Assess the morphology of the erythrocytes.
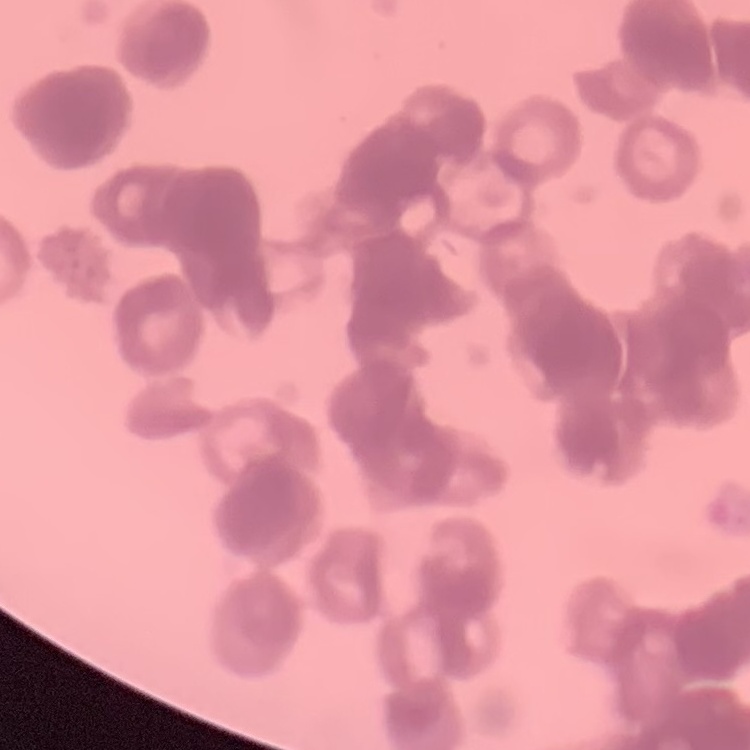
Rouleaux formation.

{
  "stain": "Field's or Giemsa",
  "image_type": "square crop of a larger photomicrograph",
  "preparation": "thin blood film"
}